State which parasite is depicted.
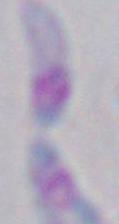

This is Toxoplasma gondii.

Summary:
  - Magnification: 1000x
  - Modality: micrograph